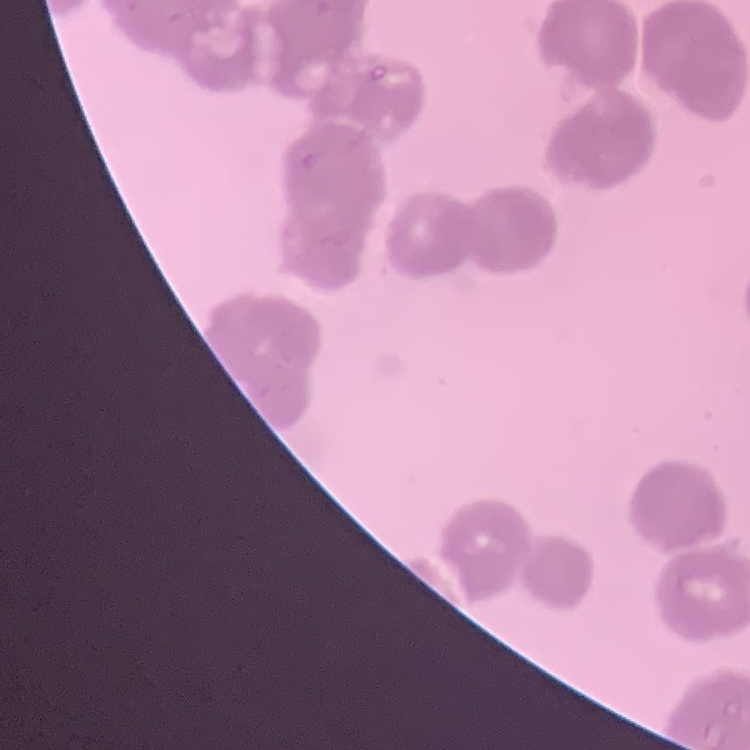
Summary:
  - Red blood cell morphology: rouleaux formation
  - Stain: Field's or Giemsa
  - Preparation: thin blood film
  - Image type: square crop of a larger photomicrograph